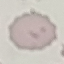

Summary:
  - Malaria status: uninfected
  - Capture: smartphone camera at the microscope eyepiece
  - Image type: cell patch, automatically extracted from a larger field of view and resized to 64 × 64 pixels
  - Preparation: thin blood film
  - Stain: Giemsa